Classify this cell by malaria status.
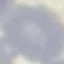
It is uninfected.

image type = cell patch, automatically extracted from a larger field of view and resized to 64 × 64 pixels
stain = Giemsa
capture = smartphone camera at the microscope eyepiece
preparation = thin smear